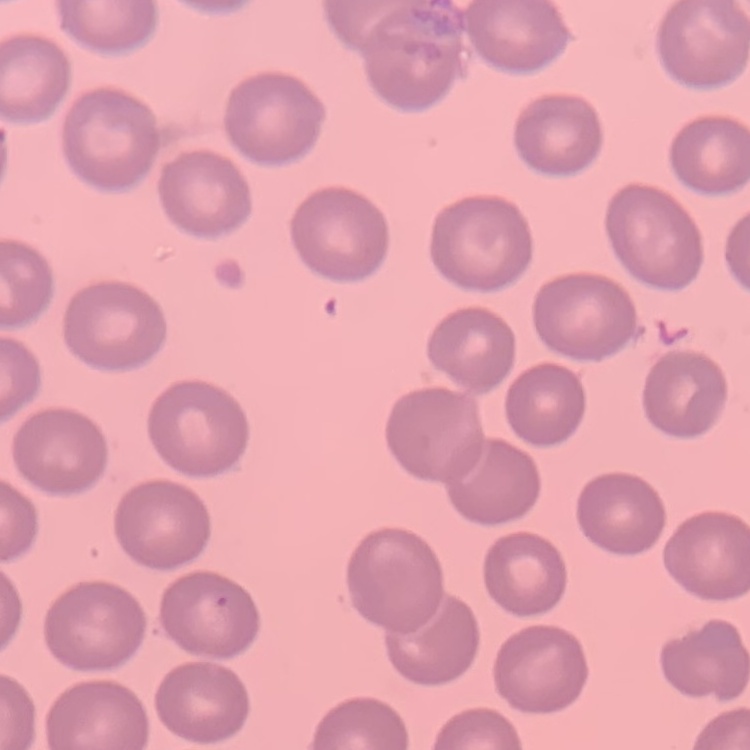

erythrocyte morphology = no rouleaux formation
image type = square crop of a larger photomicrograph
stain = Field's or Giemsa
preparation = thin peripheral smear